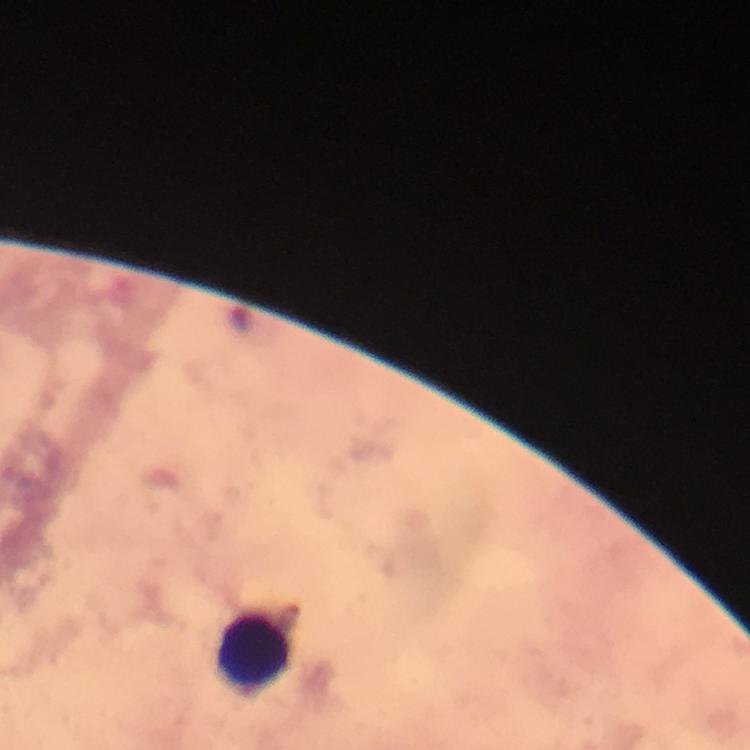

Approximate centers as {x, y} in pixels.
Summary:
  - Leukocyte locations: {253, 655}
  - Context: from a diagnostic examination for malaria
  - Preparation: thick blood smear
  - Magnification: 100x
  - Capture: smartphone photograph through a microscope
  - Stain: Giemsa
  - Plasmodium parasites: none seen
  - Image size: 750×750 pixels
  - Immersion oil: applied
  - Cropped from: a single field of view